Give the position of every malaria parasite.
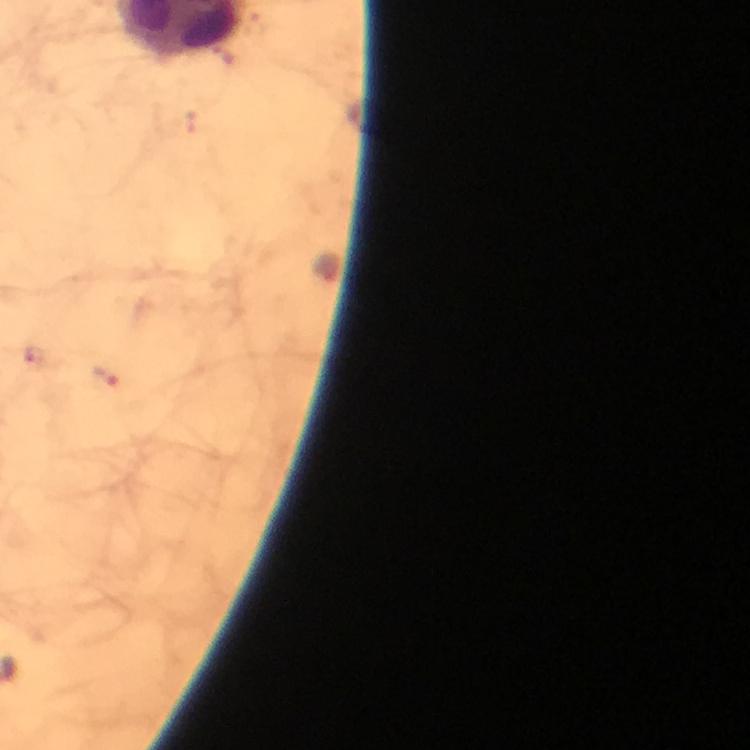
Approximate centers as {x, y} in pixels.
Malaria parasites: {323, 267}, {105, 375}.

magnification = 100x
stain = Giemsa
cropped from = one field of view
context = from a malaria diagnostic workup
capture = smartphone mounted on the microscope
immersion oil = applied
preparation = thick smear
image size = 750×750 pixels